Classify this cell by malaria status.
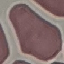
Uninfected.

Summary:
  - Image type: cell patch, automatically extracted from a larger field of view and resized to 64 × 64 pixels
  - Stain: Giemsa
  - Preparation: thin blood film
  - Capture: smartphone through the microscope eyepiece